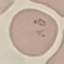

Summary:
  - Malaria status: parasitized
  - Stain: Giemsa
  - Image type: cell patch, automatically extracted from a larger field of view and resized to 64 × 64 pixels
  - Preparation: thin blood smear
  - Capture: smartphone through the microscope eyepiece